Locate every malaria parasite.
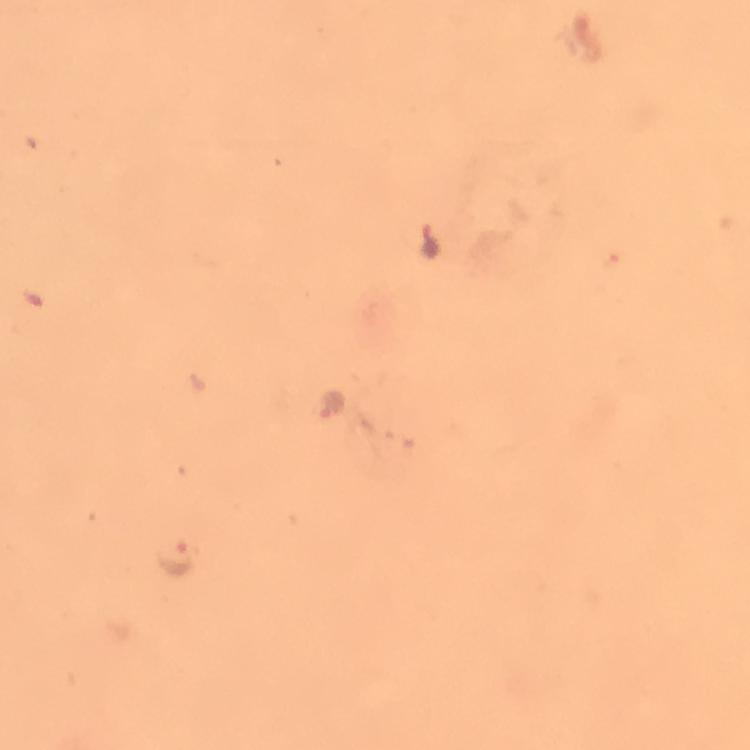
Approximate centers as (x, y) in pixels.
Malaria parasites: (332, 404), (175, 558).

Summary:
  - Magnification: 100x
  - Immersion oil: applied
  - Context: from a malaria diagnostic workup
  - Cropped from: a single field of view
  - Image size: 750×750 pixels
  - Preparation: thick smear
  - Stain: Giemsa
  - Capture: smartphone camera through the microscope